Name the blood parasite species.
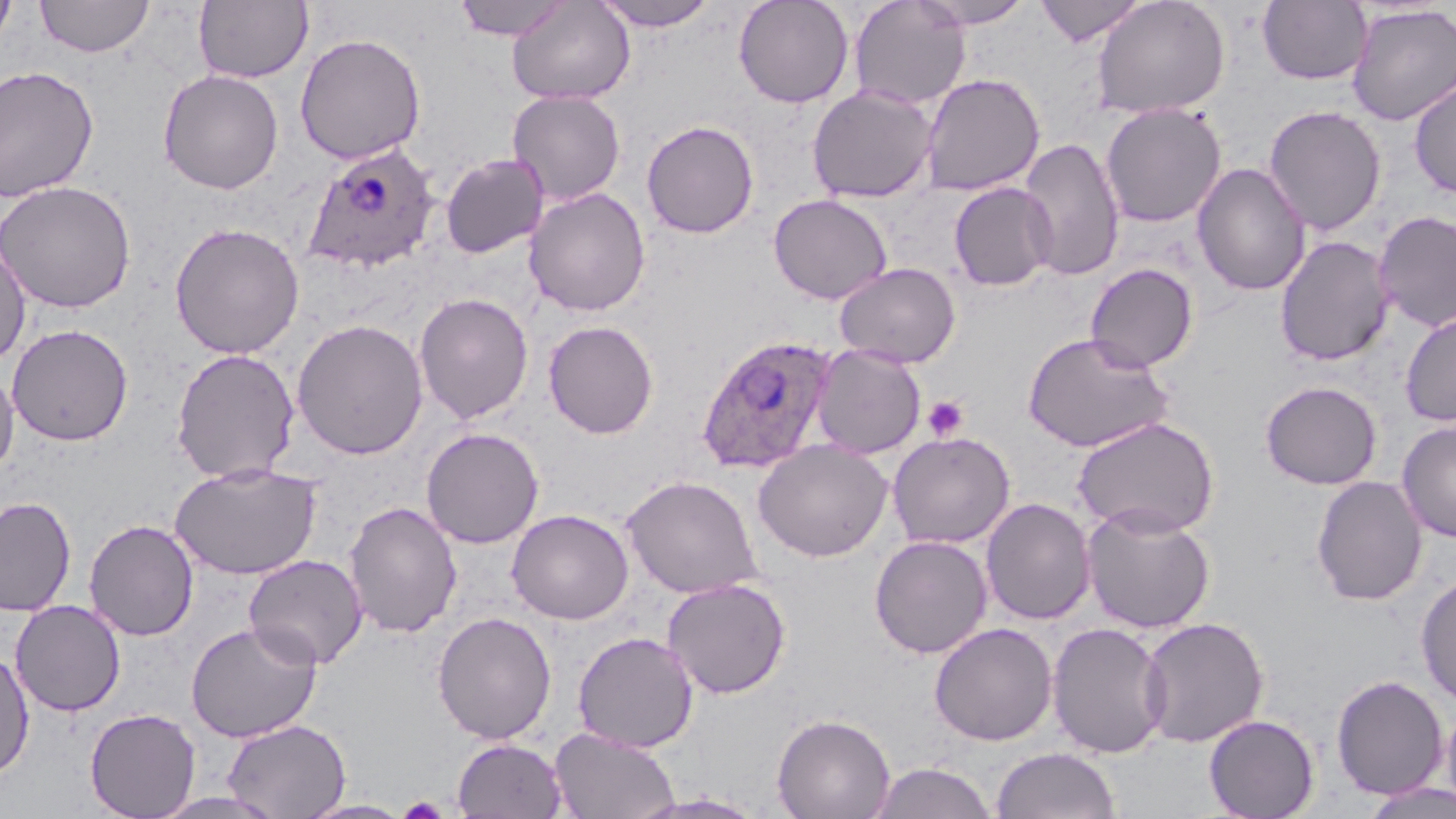

Plasmodium ovale.

Summary:
  - Coordinate format: approximate bounding boxes as (x1,y1)-(x2,y2) corner pairs in pixels
  - Platelet locations: (922,396)-(969,441), (397,795)-(450,818)
  - Uninfected red blood cell locations: (1,0)-(17,53), (35,0)-(154,57), (194,0)-(313,84), (453,0)-(572,42), (507,0)-(635,104), (733,0)-(855,108), (849,0)-(971,110), (912,0)-(1035,28), (1035,0)-(1148,46), (1091,0)-(1230,119), (591,1)-(720,31), (1257,1)-(1373,85), (1346,4)-(1456,126), (294,33)-(426,164), (0,66)-(99,202), (157,69)-(284,194), (920,72)-(1045,196), (1409,78)-(1456,199), (807,84)-(939,203), (507,89)-(626,206), (1100,103)-(1226,228), (1263,105)-(1386,235), (641,119)-(759,238), (1018,137)-(1125,282), (440,153)-(549,259), (1192,162)-(1311,297), (0,180)-(136,313), (949,182)-(1057,291), (524,187)-(651,316), (768,193)-(892,303), (1374,210)-(1456,332), (168,222)-(305,359), (1275,235)-(1395,367), (0,241)-(31,367), (835,262)-(961,367), (1085,263)-(1198,372), (413,292)-(534,425), (1399,310)-(1456,427), (291,318)-(428,459), (542,320)-(658,439), (7,324)-(133,446), (1022,332)-(1175,452), (812,344)-(926,458), (170,348)-(300,484), (0,366)-(19,476), (1260,380)-(1383,490), (1072,416)-(1220,539), (1397,421)-(1456,542), (421,427)-(544,548), (887,431)-(1015,549), (753,440)-(893,562), (169,461)-(322,579), (621,475)-(763,598), (1311,475)-(1428,606), (0,496)-(76,617), (981,497)-(1095,625), (344,501)-(463,639), (1081,504)-(1216,634), (506,509)-(634,625), (84,519)-(199,641), (868,534)-(993,658), (243,554)-(369,670), (1415,572)-(1456,707), (662,578)-(791,699), (10,599)-(126,716), (431,612)-(557,744), (1138,616)-(1270,748), (186,621)-(322,743), (1046,621)-(1171,758), (929,622)-(1058,746), (572,631)-(698,752), (0,648)-(35,781), (1331,674)-(1449,800), (1441,699)-(1456,815), (84,708)-(200,819), (772,712)-(896,819), (1203,714)-(1319,819), (222,718)-(351,819), (549,727)-(681,819), (452,737)-(569,818), (991,746)-(1121,819), (868,762)-(999,819), (1360,780)-(1456,819), (148,791)-(288,819), (633,793)-(769,818), (297,799)-(415,819)
  - Plasmodium ovale-infected red blood cell locations: (303,142)-(440,274), (695,334)-(838,475)
  - Stain: May-Grünwald-Giemsa
  - Modality: light microscopy
  - Magnification: 1000x
  - Image size: 1456×819 pixels
  - Field of view: single
  - Preparation: thin blood film